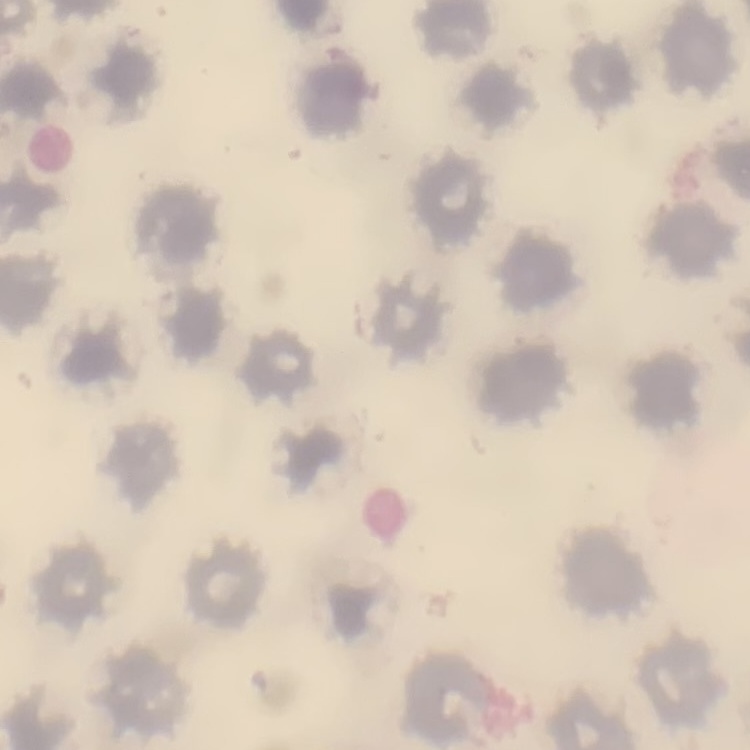
The erythrocytes exhibit no rouleaux formation. Stained with either Field's or Giemsa. Thin peripheral smear. Square crop of a larger photomicrograph.